Assess this cell for malaria.
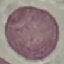

It is uninfected.

Thin blood smear. Photographed with a smartphone camera at the microscope eyepiece. Cell patch, automatically extracted from a larger field of view and resized to 64 × 64 pixels. Giemsa stain.